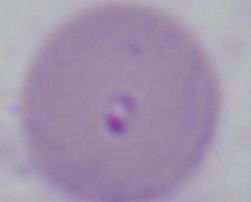

magnification = 1000x
identification = Babesia
modality = photomicrograph